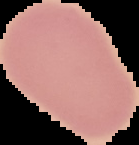

{
  "image_size": "139×145 pixels",
  "image_type": "segmented cell region with the area outside set to black",
  "preparation": "thin blood smear",
  "malaria_status": "uninfected"
}